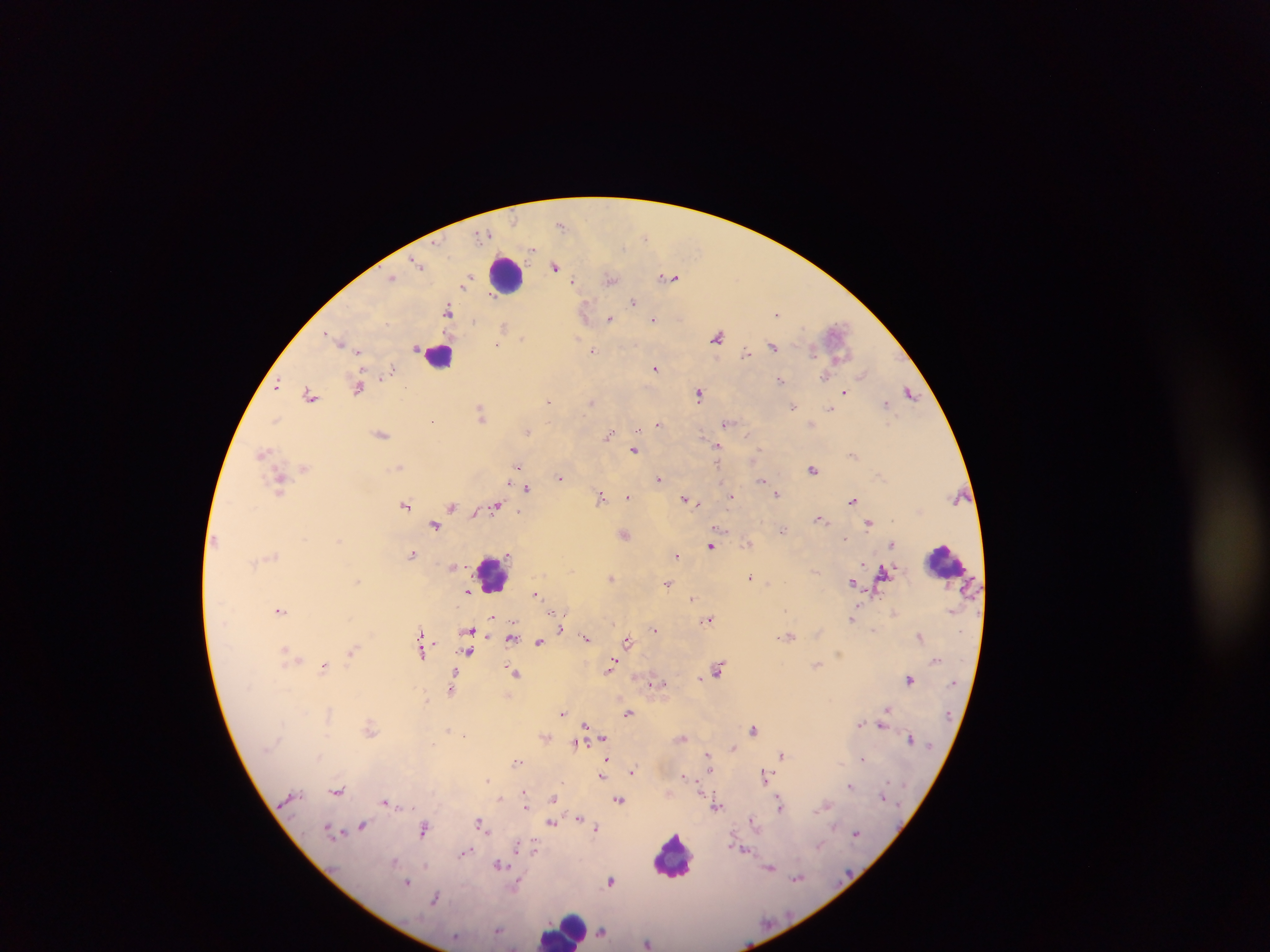

{
  "leukocyte_locations": "approximate centers as [x, y] in pixels: [508, 275], [439, 355], [945, 559], [493, 574], [673, 855], [564, 928]",
  "malaria_parasite_locations": "approximate centers as [x, y] in pixels: [561, 224], [644, 237], [533, 250], [420, 265], [555, 267], [392, 277], [669, 277], [572, 280], [610, 280], [491, 296], [633, 302], [585, 311], [448, 312], [778, 313], [610, 319], [653, 319], [473, 322], [504, 325], [835, 329], [327, 333], [717, 337], [523, 338], [337, 339], [497, 345], [774, 346], [416, 347], [593, 350], [359, 351], [746, 352], [813, 352], [392, 368], [656, 368], [862, 374], [825, 377], [780, 380], [277, 383], [358, 387], [406, 387], [910, 392], [699, 393], [845, 393], [310, 395], [549, 400], [590, 401], [886, 404], [793, 406], [830, 408], [481, 413], [276, 419], [726, 423], [658, 424], [526, 431], [382, 434], [610, 434], [746, 435], [716, 445], [635, 450], [264, 452], [518, 466], [399, 467], [813, 469], [560, 477], [658, 477], [762, 480], [280, 481], [527, 489], [777, 494], [601, 496], [628, 496], [732, 496], [685, 498], [691, 500], [853, 501], [696, 503], [406, 504], [452, 506], [496, 506], [520, 511], [820, 519], [868, 523], [435, 525], [782, 530], [625, 535], [845, 538], [215, 540], [891, 544], [711, 546], [412, 554], [275, 555], [676, 555], [453, 565], [815, 571], [883, 573], [750, 576], [612, 577], [358, 581], [853, 582], [668, 583], [469, 592], [536, 594], [692, 598], [280, 610], [493, 618], [709, 619], [853, 619], [561, 629], [470, 630], [655, 630], [873, 631], [421, 633], [919, 636], [586, 637], [789, 637], [512, 638], [627, 640], [540, 642], [352, 651], [468, 651], [285, 654], [422, 654], [817, 664], [611, 666], [324, 667], [719, 669], [514, 673], [454, 675], [700, 678], [910, 679], [650, 684], [664, 684], [452, 689], [888, 709], [562, 713], [628, 713], [860, 724], [586, 725], [882, 725], [447, 729], [370, 730], [753, 730], [603, 737], [683, 738], [910, 738], [575, 742], [732, 748], [709, 754], [782, 755], [862, 758], [606, 759], [517, 762], [710, 770], [634, 771], [764, 774], [683, 775], [602, 776], [488, 779], [850, 785], [523, 790], [338, 791], [883, 796], [500, 798], [554, 798], [619, 800], [388, 802], [779, 803], [717, 806], [526, 807], [579, 819], [753, 821], [551, 823], [480, 824], [363, 825], [424, 828], [595, 828], [331, 832], [856, 833], [519, 846], [533, 848], [465, 852], [395, 861], [498, 863], [771, 868], [797, 878], [611, 881], [407, 882], [516, 885], [435, 898], [498, 929], [601, 932], [648, 942]",
  "image_size": "1270×952 pixels",
  "field_of_view": "single",
  "country": "Ghana",
  "preparation": "thick blood film",
  "capture": "mobile-phone photograph through a microscope"
}